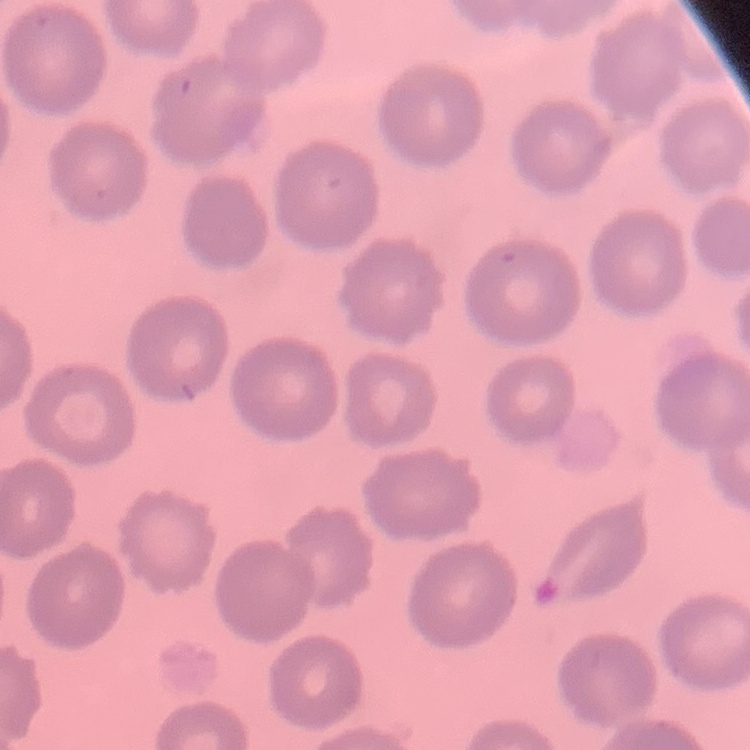

Summary:
  - Erythrocyte morphology: no rouleaux formation
  - Stain: Field's or Giemsa
  - Image type: one tile cut from a larger photomicrograph
  - Preparation: thin blood smear